Assess for malaria.
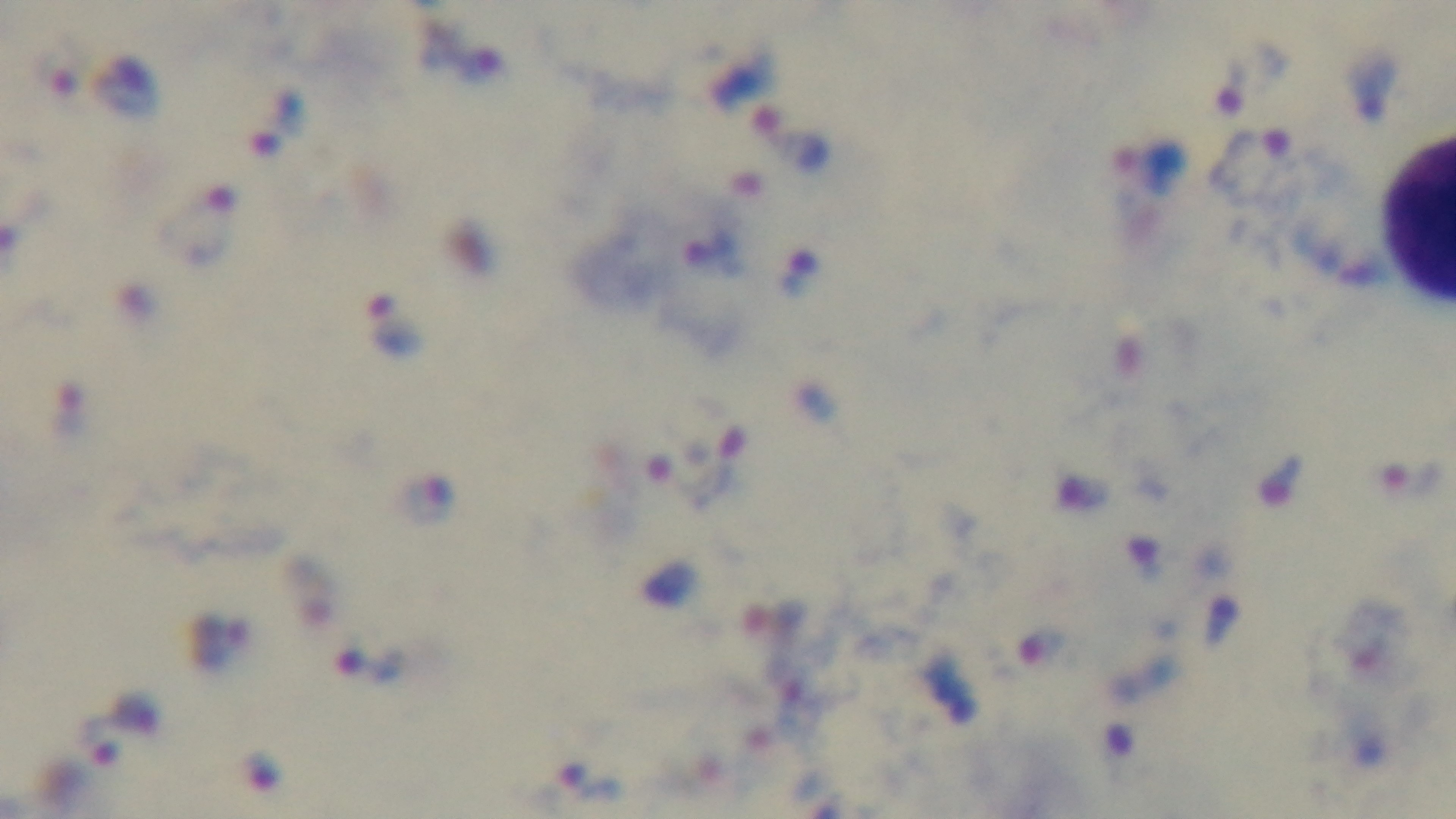
Infected.

Captured with a mounted 4K digital camera. Giemsa-stained. Single field of view. Oil-immersion objective, 100x. Photomicrograph. Preparation: thick blood film.